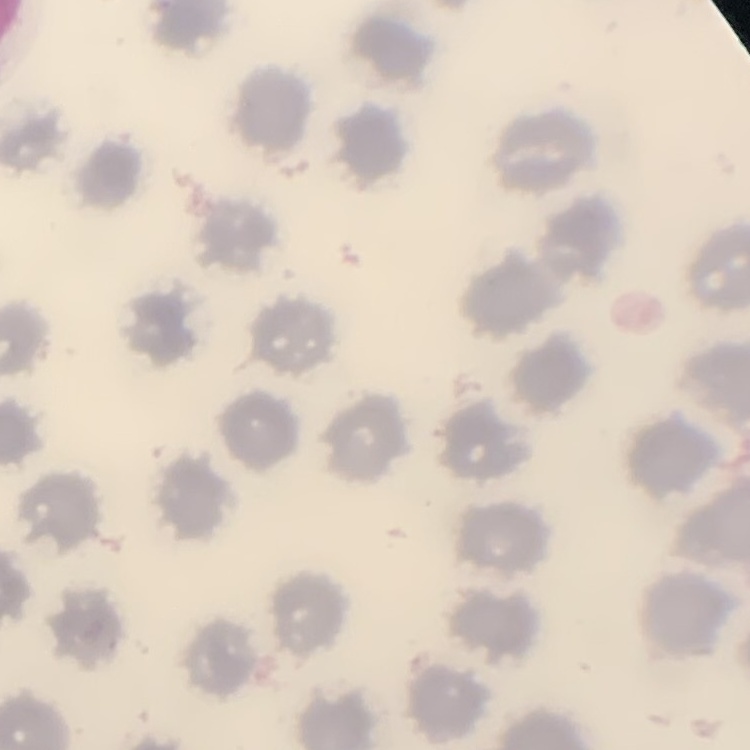

Summary:
  - Erythrocyte morphology: no rouleaux formation
  - Preparation: thin blood smear
  - Stain: Field's or Giemsa
  - Image type: one tile cut from a larger photomicrograph